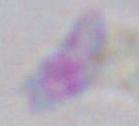
Toxoplasma gondii is seen. Photomicrograph. Captured at 1000x magnification.